Give the extent of all uninfected red blood cells.
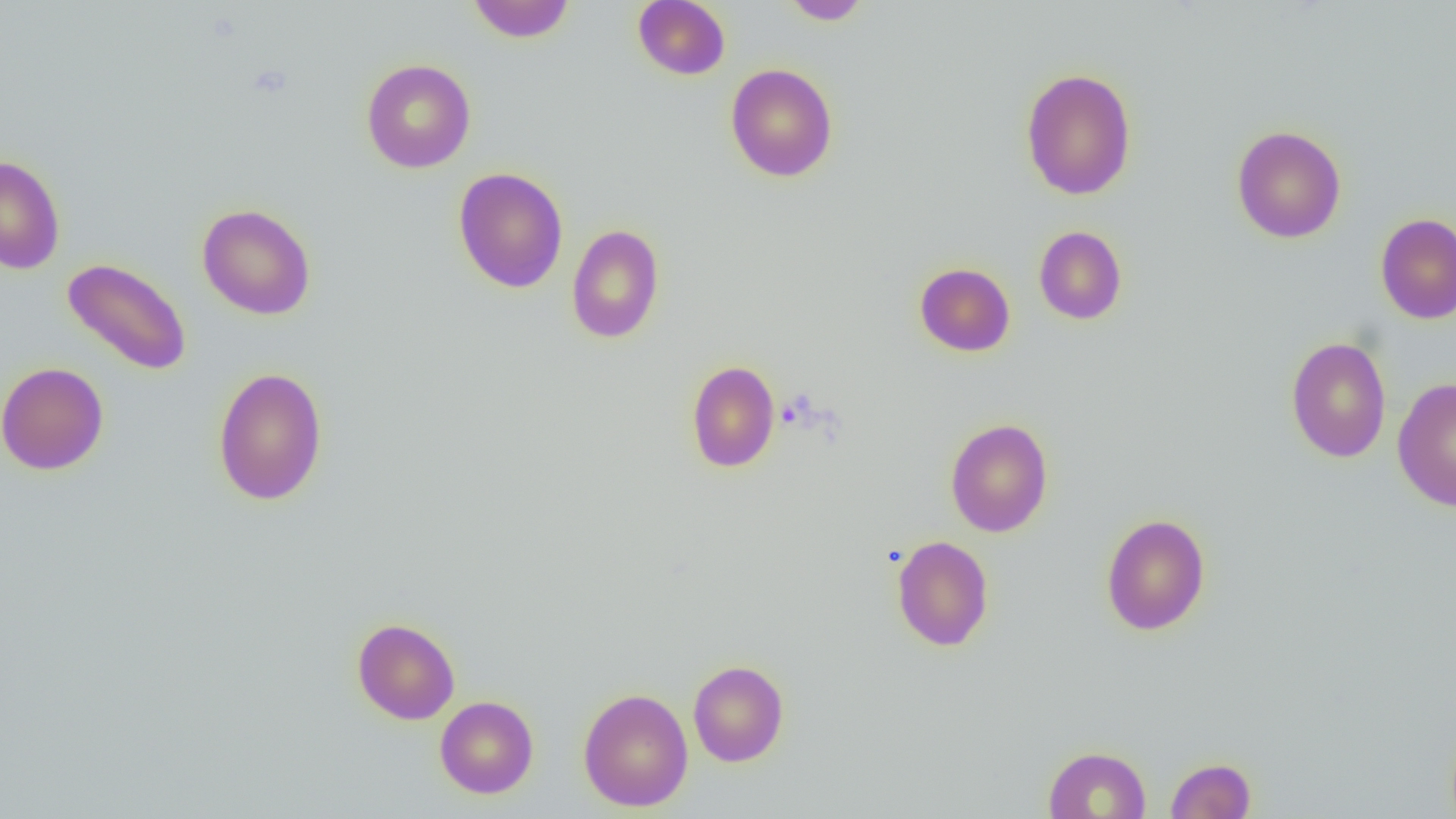

Approximate bounding boxes as (x1, y1, x2, y2) in pixels.
Uninfected red blood cells: (467, 0, 575, 43), (632, 0, 731, 80), (781, 1, 872, 24), (361, 58, 476, 173), (724, 63, 838, 182), (1020, 67, 1137, 200), (1231, 125, 1346, 243), (0, 154, 66, 275), (452, 166, 568, 293), (197, 203, 316, 320), (1375, 212, 1456, 325), (567, 224, 665, 344), (1033, 225, 1127, 325), (62, 257, 192, 376), (914, 262, 1016, 357), (1286, 336, 1392, 463), (686, 360, 780, 473), (0, 361, 109, 475), (212, 366, 328, 506), (1392, 377, 1456, 512), (945, 417, 1054, 537), (1100, 513, 1211, 635), (892, 535, 994, 652), (351, 618, 460, 724), (688, 660, 789, 767), (578, 687, 693, 811), (435, 695, 538, 798), (1043, 745, 1151, 818), (1166, 757, 1256, 818).

Slide-level diagnosis: no evidence of blood parasites. Thin blood smear. Optical microscopy. One field of a larger specimen. Captured at 1000x magnification. Image is 1456×819 pixels.